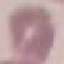
Summary:
  - Malaria status: uninfected
  - Capture: smartphone through the microscope eyepiece
  - Image type: cell patch, automatically extracted from a larger field of view and resized to 64 × 64 pixels
  - Stain: Giemsa
  - Preparation: thin blood film